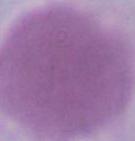
identification = red blood cell
modality = micrograph
magnification = 1000x